Give the extent of all uninfected red blood cells.
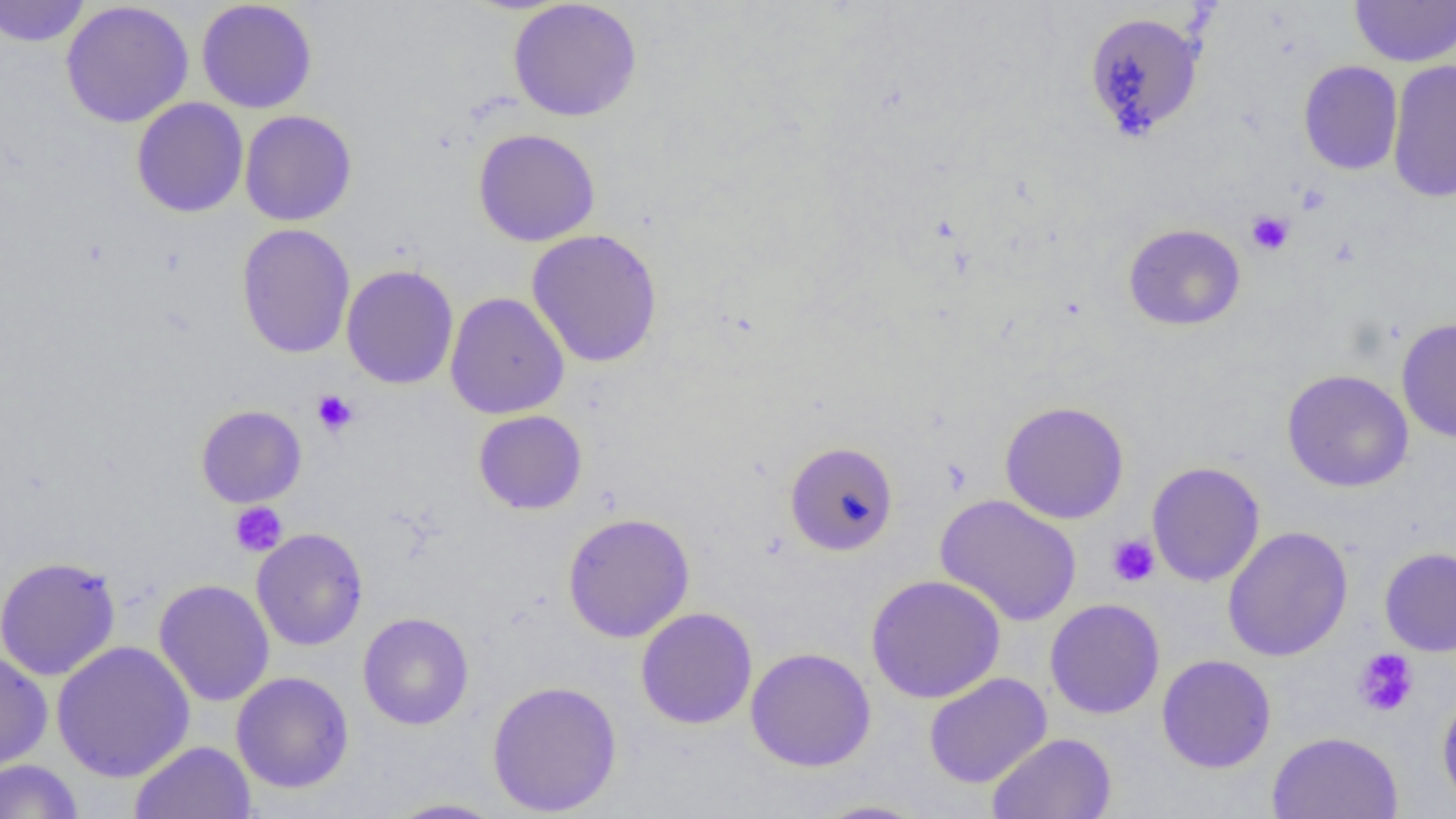

Approximate bounding boxes as named x1/y1/x2/y2 corners in pixels.
Uninfected red blood cells: (x1=0, y1=0, x2=92, y2=48), (x1=196, y1=0, x2=318, y2=114), (x1=1351, y1=0, x2=1455, y2=67), (x1=60, y1=1, x2=194, y2=129), (x1=508, y1=1, x2=642, y2=122), (x1=1083, y1=11, x2=1206, y2=141), (x1=1387, y1=59, x2=1456, y2=204), (x1=1298, y1=60, x2=1403, y2=175), (x1=131, y1=97, x2=248, y2=218), (x1=240, y1=110, x2=357, y2=226), (x1=473, y1=128, x2=600, y2=246), (x1=1123, y1=223, x2=1246, y2=331), (x1=236, y1=224, x2=356, y2=359), (x1=526, y1=228, x2=663, y2=368), (x1=341, y1=264, x2=459, y2=389), (x1=445, y1=292, x2=569, y2=419), (x1=1396, y1=317, x2=1456, y2=443), (x1=1282, y1=369, x2=1413, y2=492), (x1=999, y1=400, x2=1129, y2=524), (x1=195, y1=405, x2=307, y2=508), (x1=473, y1=410, x2=587, y2=514), (x1=784, y1=441, x2=899, y2=556), (x1=1147, y1=461, x2=1265, y2=587), (x1=934, y1=494, x2=1082, y2=627), (x1=562, y1=512, x2=695, y2=642), (x1=1223, y1=526, x2=1353, y2=662), (x1=252, y1=527, x2=368, y2=651), (x1=1378, y1=546, x2=1456, y2=657), (x1=0, y1=555, x2=121, y2=681), (x1=865, y1=574, x2=1006, y2=703), (x1=154, y1=579, x2=275, y2=707), (x1=1045, y1=598, x2=1165, y2=719), (x1=635, y1=607, x2=758, y2=729), (x1=358, y1=612, x2=474, y2=730), (x1=51, y1=640, x2=195, y2=783), (x1=744, y1=647, x2=876, y2=771), (x1=0, y1=650, x2=52, y2=772), (x1=1156, y1=654, x2=1276, y2=773), (x1=231, y1=671, x2=354, y2=793), (x1=923, y1=672, x2=1053, y2=788), (x1=486, y1=679, x2=623, y2=817), (x1=1436, y1=687, x2=1456, y2=814), (x1=1267, y1=731, x2=1404, y2=819), (x1=986, y1=732, x2=1118, y2=819), (x1=129, y1=741, x2=256, y2=819), (x1=0, y1=759, x2=84, y2=819), (x1=381, y1=797, x2=507, y2=818), (x1=809, y1=799, x2=929, y2=818).

Platelet locations: (x1=1246, y1=211, x2=1294, y2=255), (x1=312, y1=389, x2=358, y2=436), (x1=229, y1=502, x2=287, y2=557), (x1=1106, y1=533, x2=1160, y2=587), (x1=1353, y1=649, x2=1418, y2=717). Slide-level diagnosis: no evidence of blood parasites. Thin blood film. One field of a larger specimen. 1000x magnification. Image is 1456×819 pixels. Light microscopy.